Give the position of every Plasmodium parasite visible.
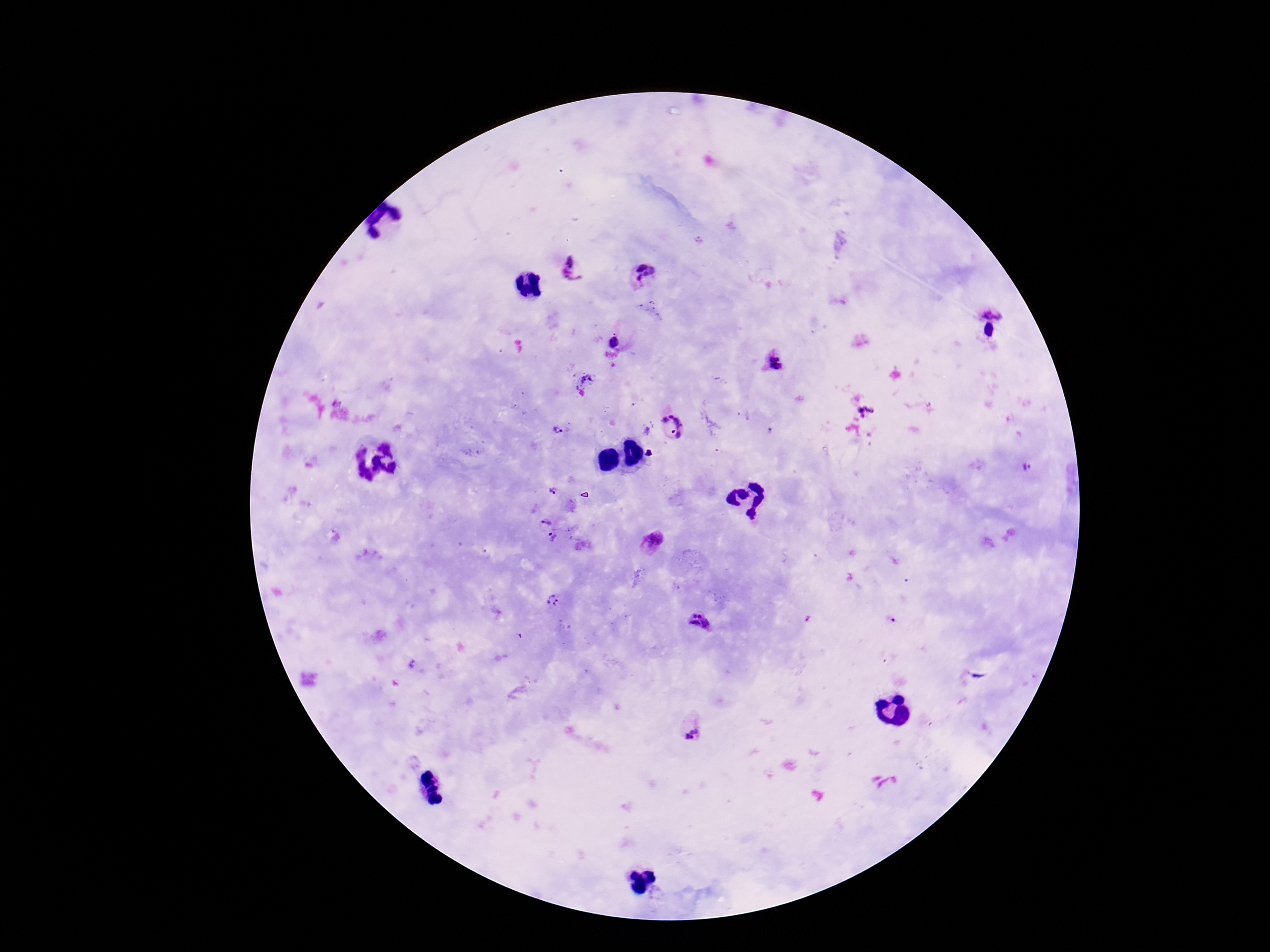
Approximate centers as [x, y] in pixels.
Plasmodium parasites: [575, 270], [644, 275], [994, 307], [991, 331], [615, 343], [775, 364], [587, 379], [868, 412], [674, 428], [558, 430], [1027, 468], [553, 492], [546, 523], [553, 539], [654, 541], [552, 600], [701, 622], [693, 734].

capture = smartphone camera through the microscope eyepiece
preparation = thick blood film
field of view = single
magnification = 100x
patient malaria status = positive
stain = Giemsa
image size = 1270×952 pixels